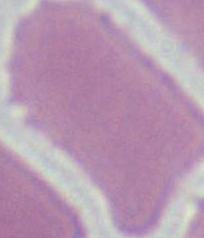
Summary:
  - Modality: photomicrograph
  - Magnification: 1000x
  - Identification: erythrocyte